Report the malaria status of this cell.
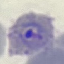

Parasitized.

{
  "capture": "smartphone through the microscope eyepiece",
  "preparation": "thin blood smear",
  "stain": "Giemsa",
  "image_type": "cell patch, automatically extracted from a larger field of view and resized to 64 × 64 pixels"
}